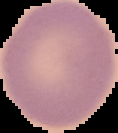 From a thin blood film. Image is 118×133 pixels. Segmented cell region on a black background. Result: no Plasmodium parasites detected.